Assess the morphology of the red blood cells.
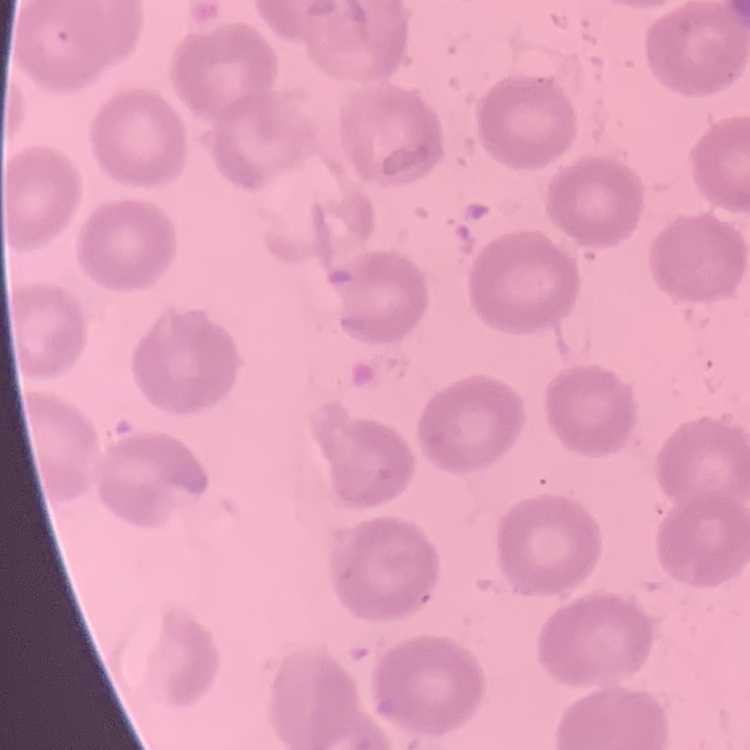

They show no rouleaux formation.

Thin blood film. Field's or Giemsa stain. One tile cut from a larger photomicrograph.